Locate and identify every blood parasite.
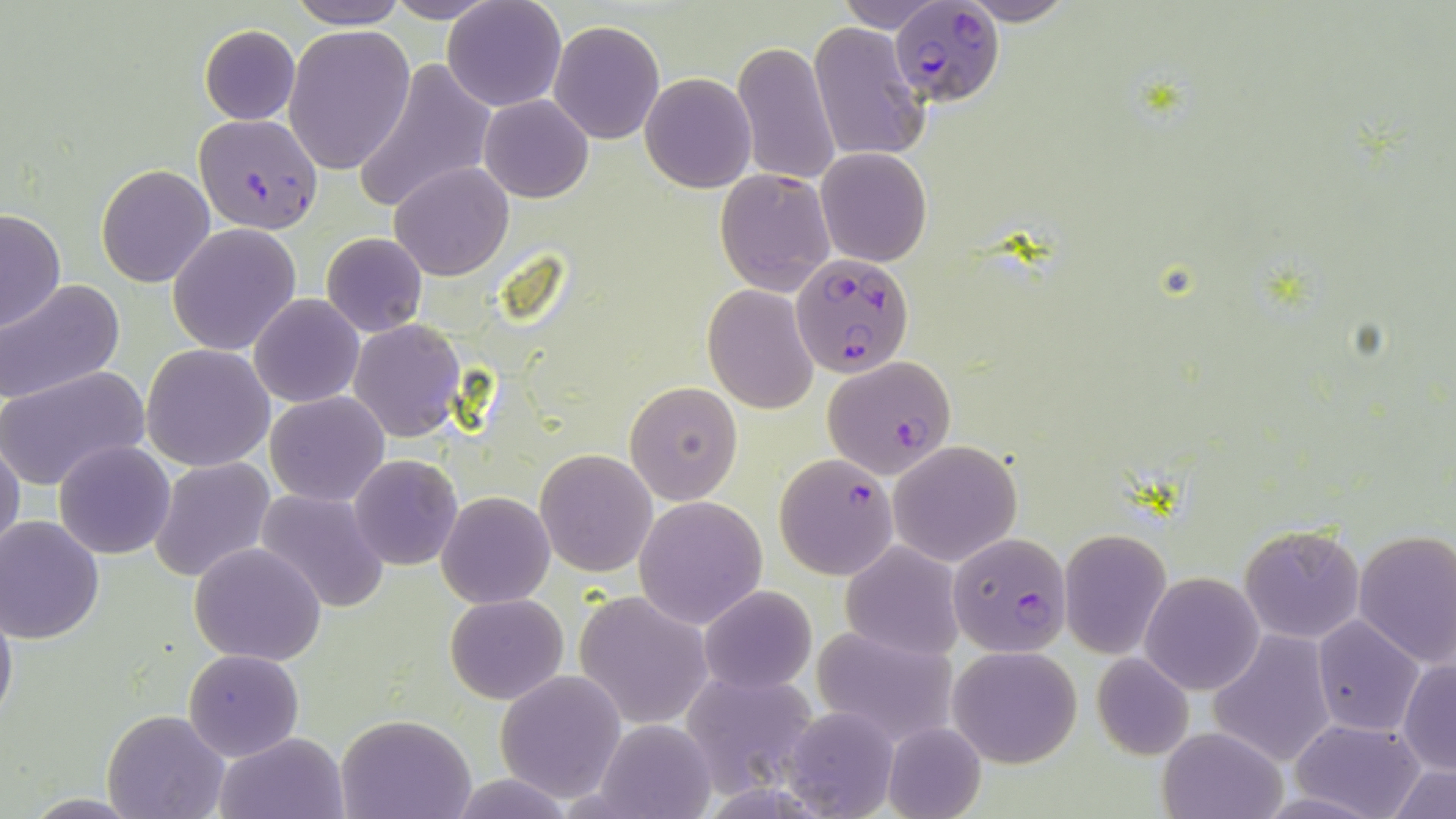
Approximate bounding boxes as [x1, y1, x2, y2] in pixels.
Plasmodium falciparum-infected red blood cells: [890, 2, 1003, 107], [193, 113, 324, 234], [790, 253, 915, 379], [821, 356, 957, 478], [773, 453, 900, 581], [948, 532, 1072, 656].
No Plasmodium ovale, Plasmodium malariae, Plasmodium vivax, Babesia divergens, or Trypanosoma brucei observed.

slide-level diagnosis = Plasmodium falciparum
magnification = 1000x
image size = 1456×819 pixels
uninfected red blood cell locations = approximate bounding boxes as [x1, y1, x2, y2] in pixels: [287, 0, 408, 28], [383, 0, 503, 23], [442, 0, 567, 112], [832, 0, 946, 33], [956, 0, 1076, 25], [550, 20, 664, 144], [808, 22, 929, 162], [198, 24, 300, 125], [284, 25, 415, 175], [733, 38, 841, 189], [352, 57, 496, 216], [641, 74, 755, 191], [479, 96, 593, 203], [816, 147, 932, 266], [391, 161, 512, 281], [96, 164, 216, 286], [715, 168, 833, 294], [0, 207, 65, 333], [167, 223, 302, 357], [320, 233, 428, 337], [0, 280, 127, 407], [702, 286, 819, 413], [250, 293, 363, 408], [349, 320, 465, 441], [141, 343, 276, 471], [0, 364, 150, 492], [625, 381, 744, 504], [267, 391, 388, 505], [0, 438, 24, 563], [888, 439, 1021, 567], [54, 440, 177, 558], [536, 449, 655, 576], [350, 455, 463, 569], [149, 456, 276, 585], [253, 486, 391, 612], [437, 493, 555, 608], [635, 495, 767, 628], [0, 515, 105, 643], [1238, 523, 1366, 644], [1058, 529, 1170, 658], [1353, 530, 1456, 668], [189, 542, 327, 665], [840, 542, 963, 660], [1140, 572, 1263, 694], [699, 585, 817, 694], [0, 590, 17, 735], [574, 591, 713, 730], [445, 594, 568, 706], [1313, 616, 1425, 736], [811, 624, 959, 748], [1209, 630, 1334, 765], [948, 645, 1082, 768], [183, 649, 303, 762], [1091, 652, 1195, 760], [1399, 659, 1455, 775], [680, 668, 823, 798], [495, 670, 627, 804], [782, 703, 898, 819], [103, 710, 228, 819], [336, 713, 475, 819], [589, 717, 719, 819], [1291, 719, 1426, 819], [881, 721, 987, 819], [1157, 726, 1284, 819], [215, 731, 349, 818], [1386, 763, 1455, 819], [18, 794, 150, 818]
stain = May-Grünwald-Giemsa
preparation = thin blood film
modality = optical microscopy
field of view = one of a larger specimen